Report the malaria status of this cell.
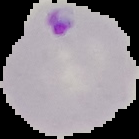

It is parasitized.

image type = segmented cell region on a black background
preparation = thin blood film
image size = 139×139 pixels